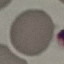 Result: no malaria parasites detected. Giemsa-stained preparation. Thin blood film. Automatically extracted cell patch, resized to 64 × 64 pixels. Acquired by smartphone through the microscope eyepiece.